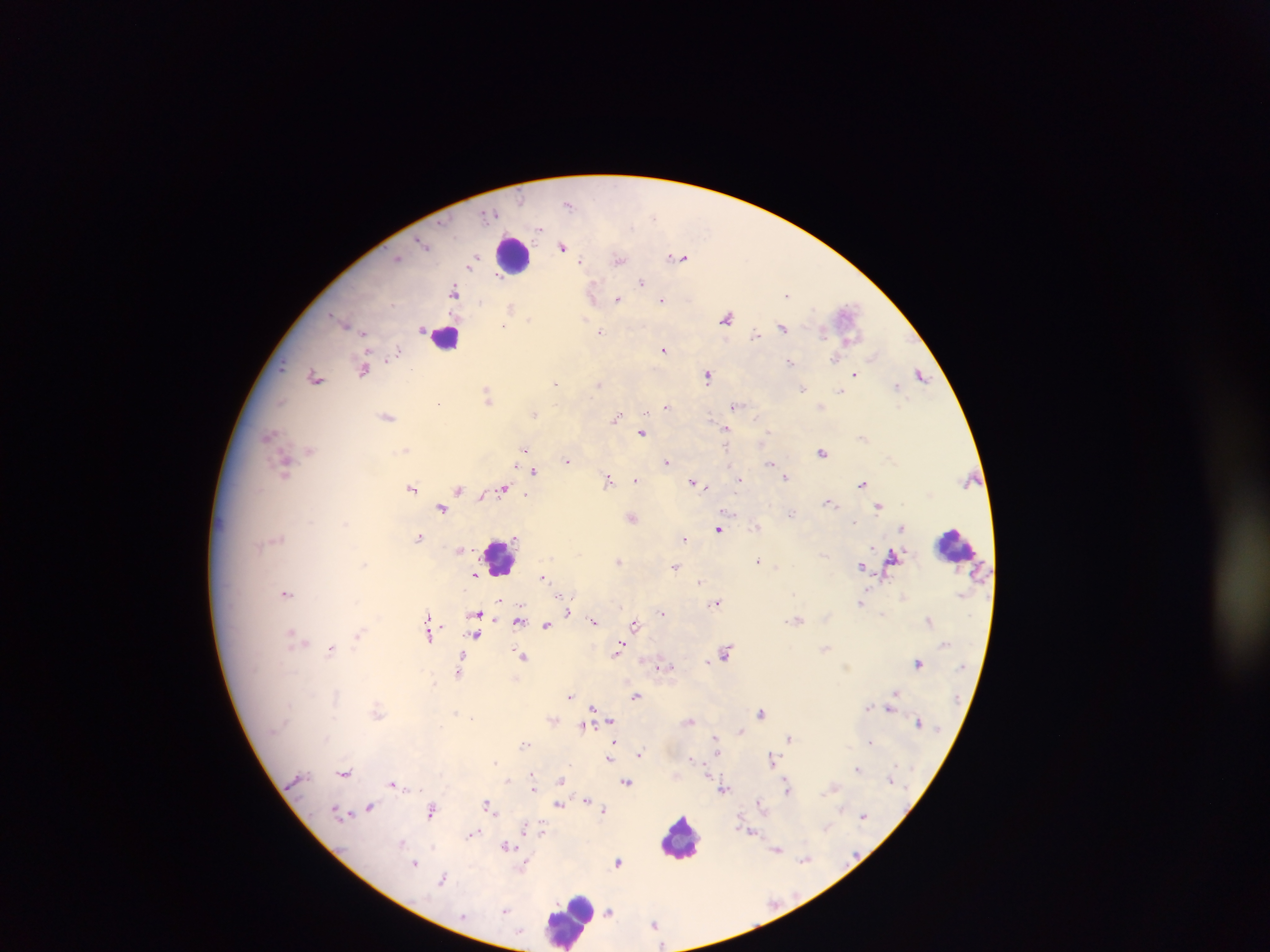

Approximate centers as x y in pixels.
Summary:
  - Malaria parasite locations: 569 205; 490 214; 653 215; 539 228; 423 243; 563 247; 397 257; 680 258; 474 259; 618 259; 580 261; 472 264; 497 277; 642 282; 454 289; 593 293; 787 294; 617 299; 662 300; 511 306; 847 312; 727 317; 530 319; 585 320; 346 323; 502 325; 782 328; 363 332; 600 332; 755 334; 664 350; 398 351; 872 356; 836 357; 791 362; 363 369; 412 370; 855 374; 921 375; 315 376; 707 376; 554 382; 599 384; 897 386; 803 389; 840 391; 487 395; 281 400; 439 402; 666 406; 735 406; 535 414; 617 416; 388 417; 756 418; 712 420; 643 433; 769 433; 726 434; 269 435; 726 446; 406 449; 524 449; 310 450; 822 452; 567 461; 667 461; 770 462; 284 465; 534 472; 785 477; 636 479; 739 479; 608 480; 693 482; 863 484; 706 485; 412 488; 502 488; 459 489; 526 495; 829 502; 879 506; 442 508; 729 513; 792 513; 633 518; 853 522; 755 526; 902 528; 719 529; 418 537; 684 538; 460 549; 893 556; 758 560; 618 561; 364 565; 861 566; 676 567; 777 567; 475 575; 543 577; 700 582; 287 593; 861 602; 715 603; 567 611; 662 612; 476 615; 594 620; 798 620; 928 620; 517 622; 547 625; 635 625; 429 631; 359 634; 292 635; 474 635; 299 641; 620 647; 331 649; 617 652; 726 652; 522 656; 708 661; 918 663; 659 667; 667 667; 459 670; 435 682; 895 692; 570 696; 636 696; 593 707; 870 707; 890 708; 377 711; 456 712; 760 712; 471 717; 610 720; 690 721; 918 722; 583 727; 741 730; 714 736; 790 737; 871 741; 614 742; 524 744; 716 750; 640 754; 610 758; 692 759; 772 759; 495 762; 857 768; 706 771; 344 772; 533 775; 508 780; 561 781; 627 782; 393 783; 787 786; 533 789; 724 790; 587 800; 760 802; 487 805; 558 805; 370 807; 431 810; 604 810; 338 811; 864 815; 826 827; 527 828; 542 831; 751 831; 472 834; 402 842; 506 846; 777 850; 804 859; 618 861; 414 863; 523 868; 443 878; 506 910; 610 912; 654 924
  - Leukocyte locations: 513 255; 447 337; 955 544; 502 556; 681 836; 568 920
  - Image size: 1270×952 pixels
  - Country: Ghana
  - Preparation: thick blood smear
  - Capture: mobile-phone photograph through a microscope
  - Field of view: single